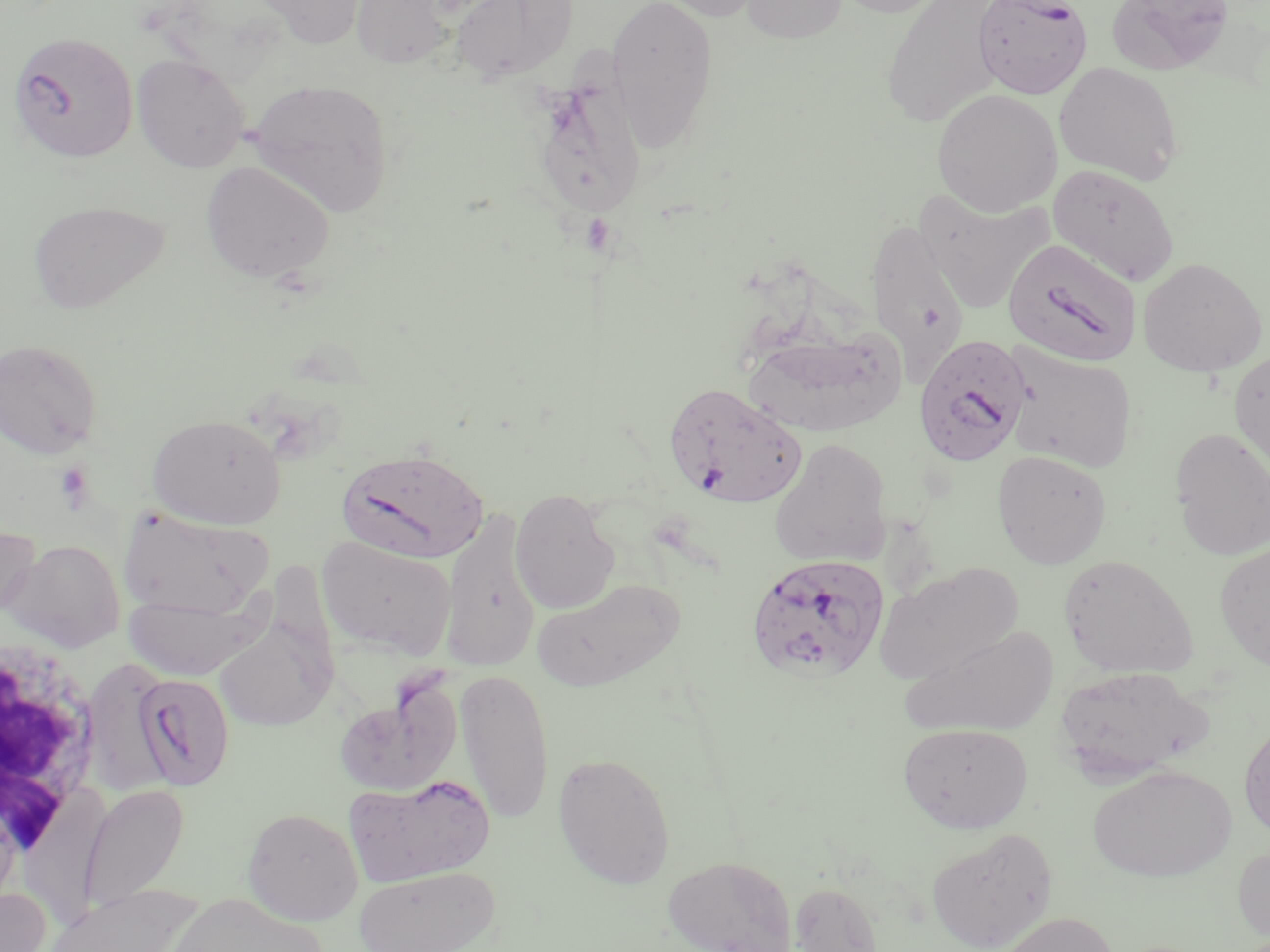
Summary:
  - Coordinate format: approximate bounding boxes as (x1, y1, x2, y2) in pixels
  - Plasmodium falciparum-infected red blood cell locations: (972, 0, 1092, 99), (7, 30, 138, 164), (1003, 237, 1141, 367), (912, 334, 1033, 468), (664, 382, 808, 509), (338, 448, 490, 565), (744, 552, 890, 685), (131, 671, 236, 791)
  - Platelet locations: (55, 461, 95, 510)
  - Uninfected red blood cell locations: (250, 0, 368, 48), (351, 0, 453, 69), (450, 0, 578, 84), (606, 0, 719, 150), (650, 0, 768, 21), (741, 0, 847, 44), (831, 0, 952, 17), (1105, 0, 1237, 76), (881, 1, 1008, 126), (131, 53, 250, 173), (1054, 62, 1184, 184), (527, 77, 648, 221), (247, 79, 395, 217), (931, 89, 1062, 215), (201, 161, 335, 284), (1048, 164, 1180, 286), (916, 192, 1054, 313), (28, 199, 170, 314), (866, 220, 969, 377), (1138, 257, 1267, 377), (742, 328, 906, 438), (0, 338, 102, 459), (1001, 343, 1138, 473), (1229, 349, 1270, 477), (147, 412, 286, 529), (1168, 428, 1270, 560), (770, 437, 892, 568), (991, 449, 1112, 569), (510, 487, 620, 614), (440, 506, 541, 671), (118, 507, 272, 618), (0, 524, 41, 620), (316, 535, 457, 661), (6, 539, 125, 651), (1214, 541, 1270, 670), (1058, 555, 1198, 678), (874, 563, 1022, 684), (534, 578, 684, 692), (124, 590, 267, 680), (213, 617, 336, 732), (900, 623, 1059, 739), (83, 660, 173, 798), (1054, 665, 1212, 783), (455, 669, 555, 825), (334, 682, 462, 798), (1239, 718, 1270, 843), (898, 722, 1033, 833), (553, 751, 676, 889), (1087, 764, 1236, 882), (345, 774, 495, 886), (77, 782, 190, 915), (242, 807, 363, 925), (926, 826, 1058, 952), (1233, 844, 1270, 944), (663, 854, 798, 952), (353, 865, 502, 952), (788, 880, 886, 951), (44, 885, 200, 952), (0, 887, 50, 952), (166, 892, 330, 952), (993, 912, 1121, 952)
  - White blood cell locations: (0, 633, 103, 865)
  - Slide-level diagnosis: Plasmodium falciparum
  - Preparation: thin blood film
  - Field of view: one of a larger specimen
  - Stain: May-Grünwald-Giemsa
  - Modality: light microscopy
  - Image size: 1270×952 pixels
  - Magnification: 1000x